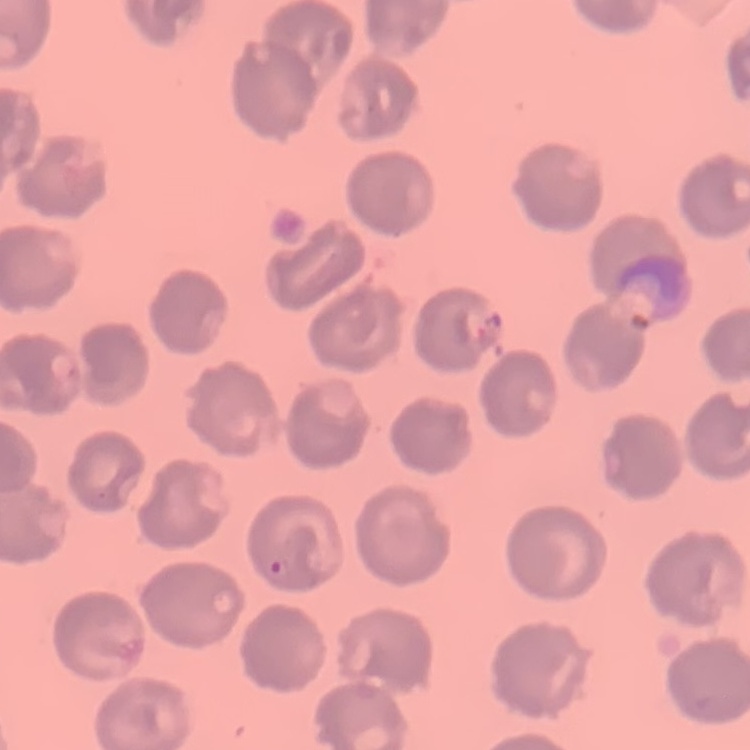

The erythrocytes show no rouleaux formation. One tile cut from a larger photomicrograph. Stained with either Field's or Giemsa. Thin blood film.